Identify the blood parasite species.
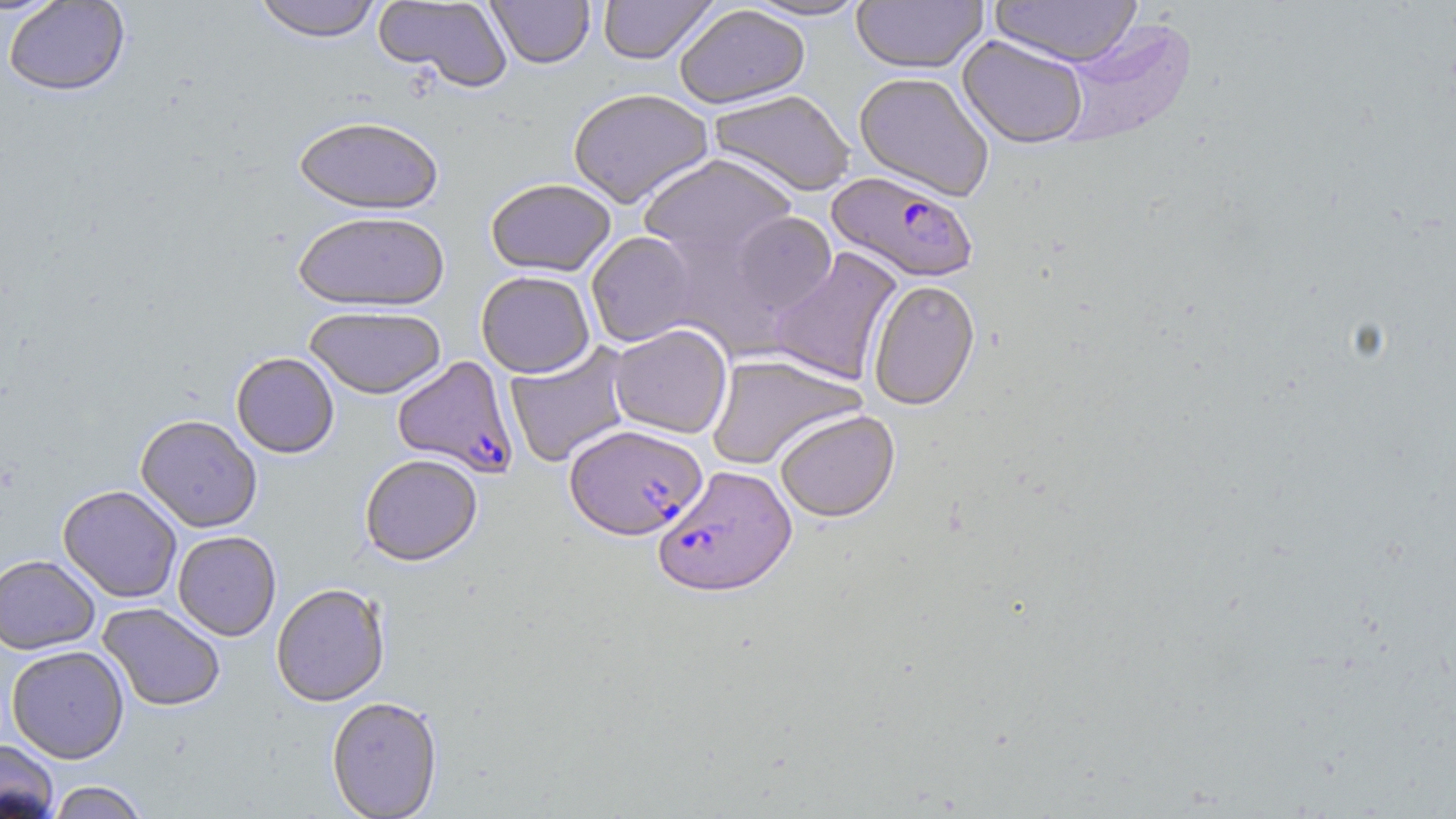
Plasmodium falciparum.

Summary:
  - Coordinate format: approximate bounding boxes as (x1,y1)-(x2,y2) corner pairs in pixels
  - Plasmodium falciparum-infected red blood cell locations: (827,171)-(979,284), (392,356)-(519,478), (564,424)-(706,540), (653,464)-(798,597)
  - Uninfected red blood cell locations: (250,0)-(383,42), (373,0)-(513,93), (485,0)-(595,69), (597,0)-(718,65), (744,0)-(871,22), (990,0)-(1142,68), (2,1)-(130,97), (851,1)-(988,74), (674,4)-(810,109), (1055,19)-(1196,152), (957,35)-(1089,149), (854,72)-(995,202), (567,88)-(714,209), (709,90)-(856,197), (293,116)-(444,214), (639,153)-(798,267), (485,177)-(616,276), (293,210)-(450,312), (727,211)-(837,317), (586,231)-(700,347), (769,247)-(902,385), (476,270)-(595,377), (868,279)-(980,411), (304,305)-(447,398), (608,323)-(733,439), (504,342)-(634,468), (231,352)-(339,458), (706,354)-(866,471), (774,409)-(900,522), (135,414)-(263,532), (359,453)-(483,566), (58,484)-(182,602), (172,530)-(282,640), (0,554)-(100,655), (271,583)-(390,706), (97,602)-(226,712), (5,644)-(129,763), (326,696)-(443,817), (0,739)-(60,819), (46,781)-(150,819)
  - Magnification: 1000x
  - Stain: May-Grünwald-Giemsa
  - Image size: 1456×819 pixels
  - Preparation: thin blood film
  - Modality: light microscopy
  - Field of view: one of a larger specimen